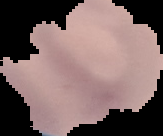

{
  "result": "no malaria parasites detected",
  "preparation": "thin blood film",
  "image_type": "cell region segmented out of the field of view; surrounding area masked to black",
  "image_size": "163×136 pixels"
}